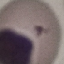
result = no malaria parasites seen
capture = smartphone camera at the microscope eyepiece
image type = cell patch, automatically extracted from a larger field of view and resized to 64 × 64 pixels
preparation = thin smear
stain = Giemsa